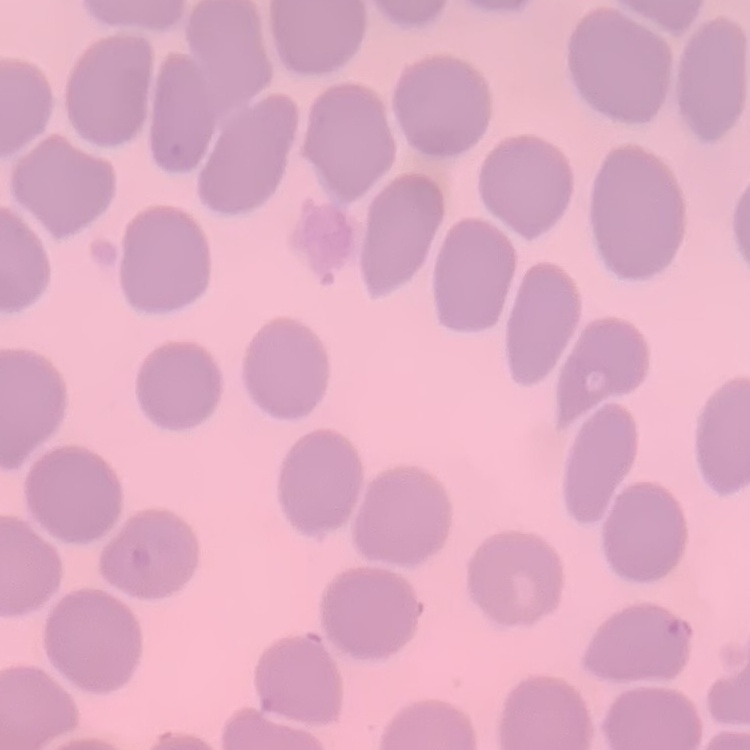
erythrocyte_morphology: no rouleaux formation
image_type: one tile cut from a larger photomicrograph
stain: Field's or Giemsa
preparation: thin blood smear